Identify the parasite.
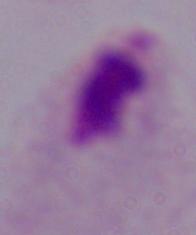

This is a trichomonad.

Summary:
  - Magnification: 1000x
  - Modality: micrograph